Identify the preparation type.
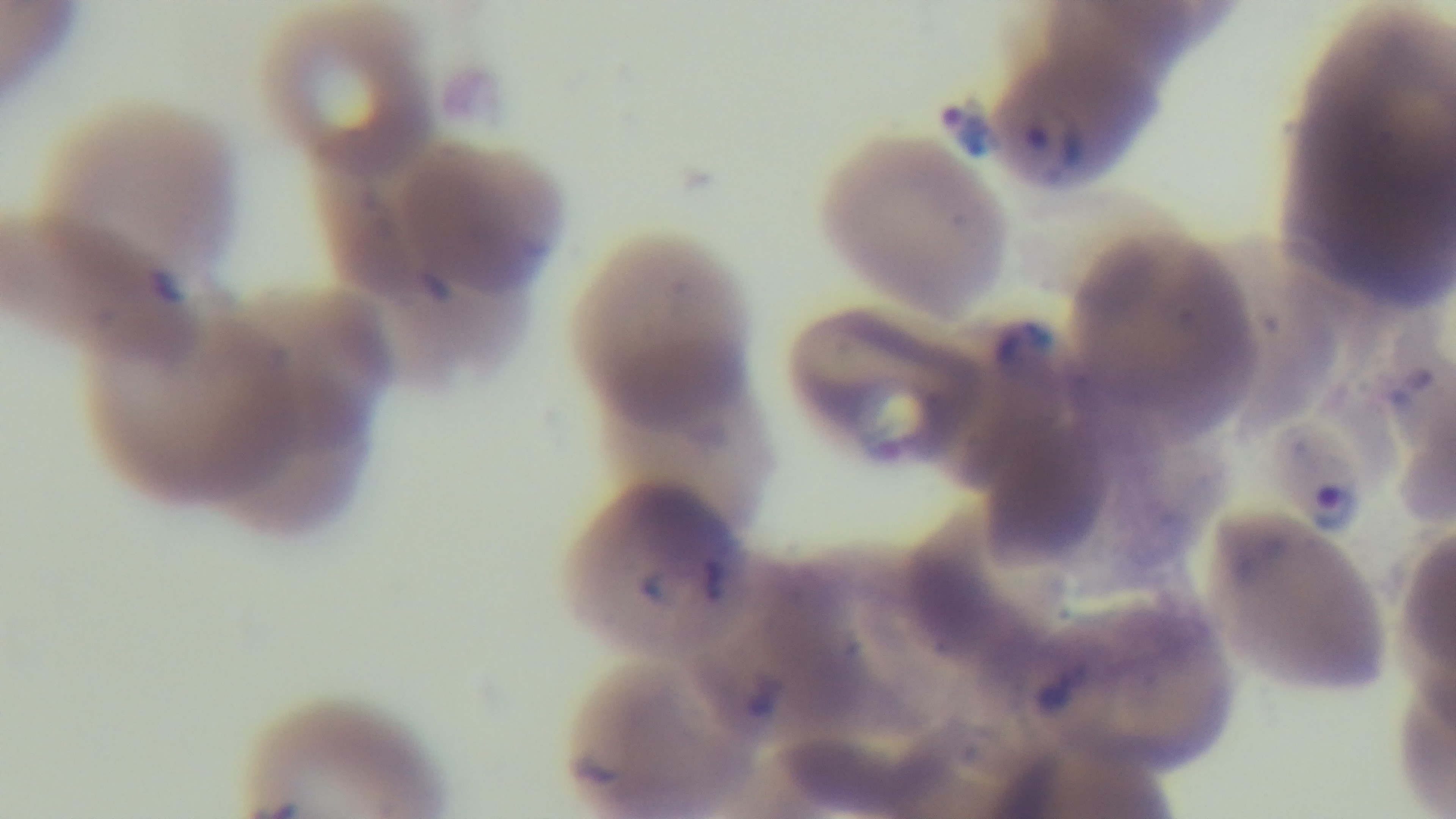

Thin.

Summary:
  - Objective: 100x oil immersion
  - Stain: Giemsa
  - Capture: mounted 4K digital camera
  - Field of view: one from the slide
  - Malaria status: positive
  - Modality: light microscopy